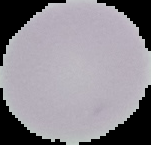
image type = segmented cell region with the area outside set to black
result = no malaria parasites seen
image size = 151×145 pixels
preparation = thin blood smear